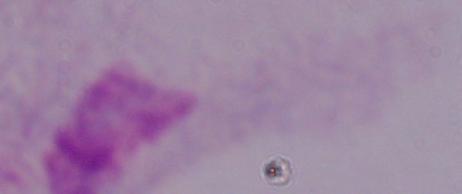

modality = photomicrograph
magnification = 1000x
identification = trichomonad